Locate every Plasmodium malariae-infected red blood cell.
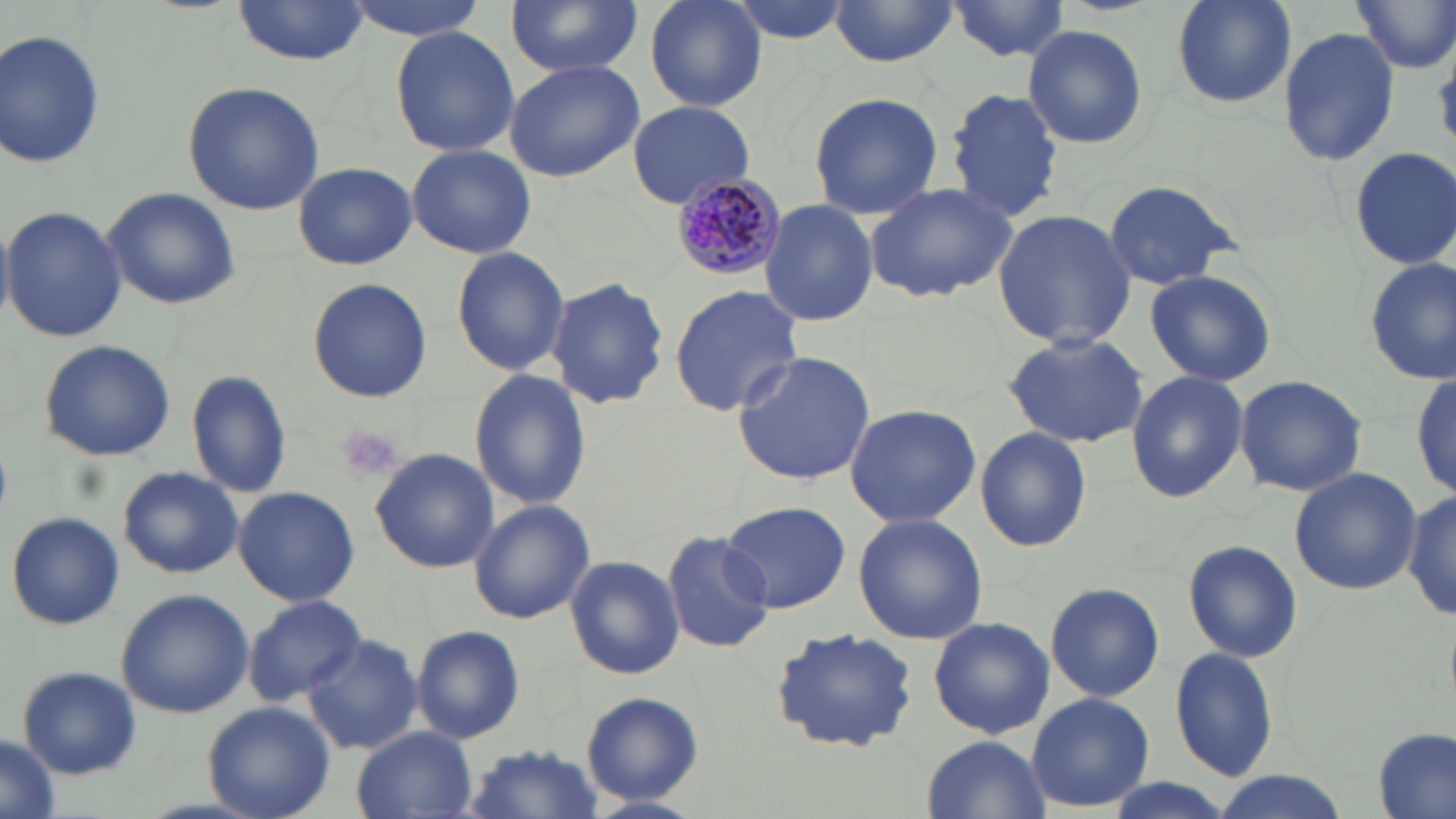
Approximate bounding boxes as named x1/y1/x2/y2 corners in pixels.
Plasmodium malariae-infected red blood cells: (x1=672, y1=174, x2=789, y2=281).

Summary:
  - Uninfected red blood cell locations: (x1=342, y1=0, x2=494, y2=40), (x1=505, y1=0, x2=644, y2=78), (x1=642, y1=0, x2=768, y2=111), (x1=723, y1=0, x2=855, y2=44), (x1=946, y1=0, x2=1072, y2=63), (x1=1168, y1=0, x2=1299, y2=108), (x1=1350, y1=0, x2=1456, y2=75), (x1=229, y1=1, x2=374, y2=65), (x1=828, y1=2, x2=958, y2=68), (x1=1022, y1=23, x2=1148, y2=151), (x1=388, y1=24, x2=521, y2=158), (x1=1277, y1=26, x2=1399, y2=167), (x1=1, y1=28, x2=107, y2=173), (x1=504, y1=58, x2=644, y2=182), (x1=181, y1=81, x2=326, y2=215), (x1=944, y1=88, x2=1064, y2=221), (x1=807, y1=91, x2=947, y2=219), (x1=626, y1=101, x2=756, y2=207), (x1=406, y1=143, x2=537, y2=260), (x1=1351, y1=144, x2=1456, y2=270), (x1=295, y1=161, x2=416, y2=270), (x1=1101, y1=177, x2=1245, y2=290), (x1=863, y1=180, x2=1018, y2=304), (x1=102, y1=187, x2=242, y2=311), (x1=760, y1=198, x2=878, y2=327), (x1=2, y1=205, x2=127, y2=343), (x1=992, y1=207, x2=1136, y2=352), (x1=450, y1=244, x2=570, y2=377), (x1=1364, y1=255, x2=1454, y2=384), (x1=1143, y1=268, x2=1278, y2=386), (x1=306, y1=277, x2=433, y2=404), (x1=546, y1=278, x2=669, y2=408), (x1=668, y1=284, x2=804, y2=416), (x1=1136, y1=284, x2=1268, y2=481), (x1=1000, y1=330, x2=1150, y2=448), (x1=39, y1=339, x2=176, y2=461), (x1=732, y1=350, x2=876, y2=485), (x1=470, y1=368, x2=591, y2=512), (x1=187, y1=369, x2=294, y2=499), (x1=1125, y1=371, x2=1249, y2=503), (x1=1411, y1=371, x2=1454, y2=502), (x1=1234, y1=374, x2=1368, y2=497), (x1=843, y1=403, x2=982, y2=529), (x1=974, y1=427, x2=1093, y2=552), (x1=370, y1=447, x2=499, y2=573), (x1=117, y1=466, x2=244, y2=578), (x1=1288, y1=467, x2=1421, y2=595), (x1=233, y1=486, x2=360, y2=606), (x1=1404, y1=487, x2=1456, y2=623), (x1=469, y1=500, x2=595, y2=624), (x1=721, y1=500, x2=849, y2=613), (x1=7, y1=512, x2=123, y2=629), (x1=852, y1=513, x2=988, y2=646), (x1=662, y1=531, x2=773, y2=654), (x1=1181, y1=538, x2=1305, y2=664), (x1=565, y1=555, x2=685, y2=681), (x1=1043, y1=580, x2=1165, y2=702), (x1=116, y1=589, x2=254, y2=719), (x1=244, y1=594, x2=365, y2=706), (x1=928, y1=615, x2=1054, y2=739), (x1=411, y1=625, x2=524, y2=744), (x1=770, y1=626, x2=918, y2=754), (x1=303, y1=634, x2=423, y2=757), (x1=1170, y1=645, x2=1280, y2=782), (x1=17, y1=666, x2=143, y2=779), (x1=1025, y1=690, x2=1154, y2=811), (x1=583, y1=692, x2=703, y2=806), (x1=204, y1=702, x2=336, y2=819), (x1=351, y1=727, x2=478, y2=818), (x1=1373, y1=729, x2=1453, y2=819), (x1=921, y1=734, x2=1049, y2=818), (x1=0, y1=737, x2=59, y2=819), (x1=460, y1=744, x2=607, y2=819), (x1=1209, y1=772, x2=1352, y2=819)
  - Platelet locations: (x1=335, y1=425, x2=405, y2=482)
  - Slide-level diagnosis: Plasmodium malariae
  - Magnification: 1000x
  - Stain: May-Grünwald-Giemsa
  - Image size: 1456×819 pixels
  - Preparation: thin blood film
  - Field of view: single
  - Modality: optical microscopy